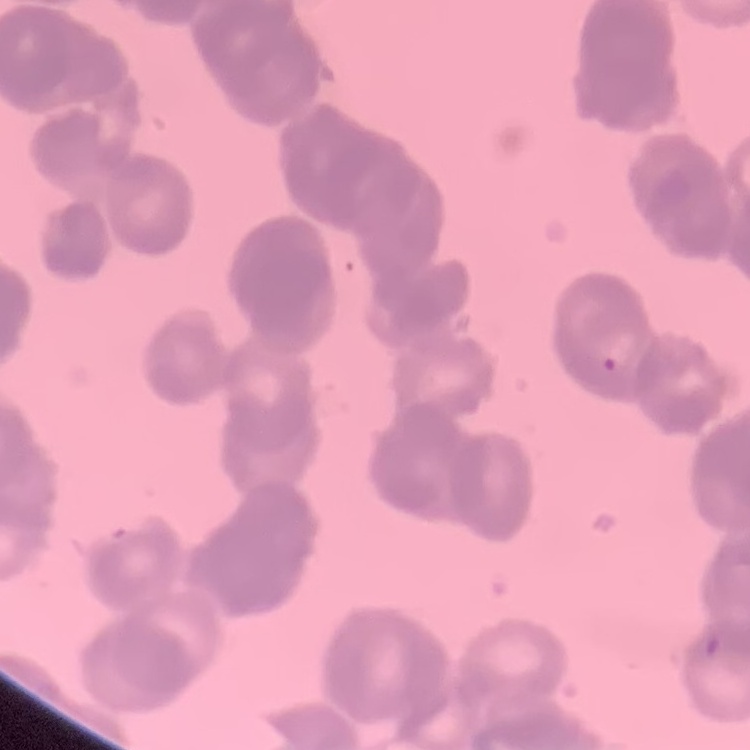

Summary:
  - Erythrocyte morphology: rouleaux formation
  - Image type: one tile cut from a larger photomicrograph
  - Preparation: thin peripheral smear
  - Stain: Field's or Giemsa